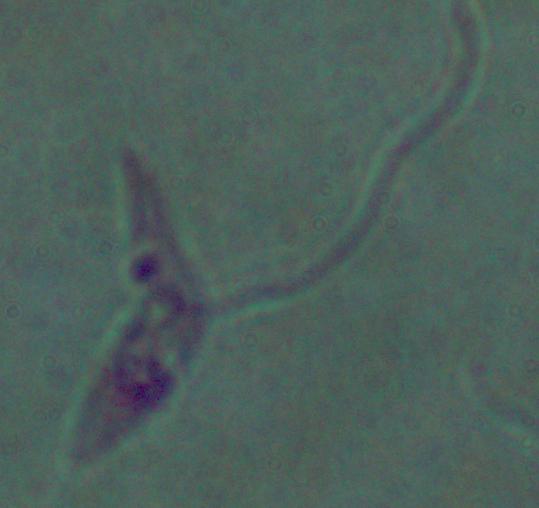
modality = photomicrograph
identification = Leishmania
magnification = 1000x